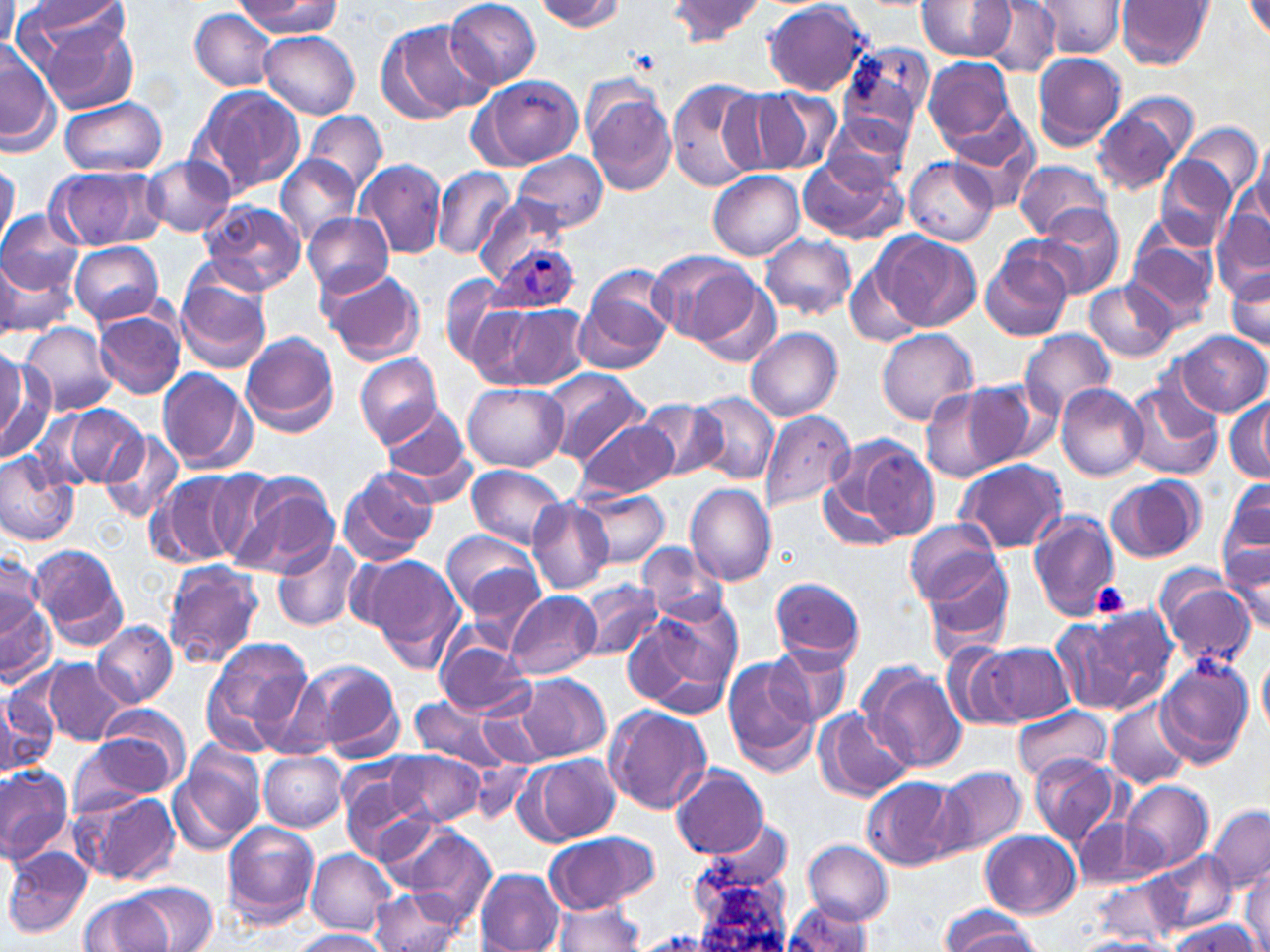

slide-level diagnosis = Plasmodium ovale
field of view = single
uninfected red blood cell locations = approximate bounding boxes as (x1,y1)-(x2,y2) corner pairs in pixels: (445,0)-(541,88), (534,0)-(626,32), (667,0)-(766,45), (1117,0)-(1213,70), (234,1)-(343,37), (917,1)-(1015,61), (980,1)-(1062,76), (1030,1)-(1125,59), (18,2)-(132,58), (763,2)-(871,95), (1243,2)-(1270,43), (189,9)-(281,92), (32,16)-(139,114), (382,18)-(492,122), (261,31)-(361,117), (0,41)-(60,158), (839,49)-(929,145), (1031,52)-(1127,151), (923,57)-(1018,149), (476,75)-(583,169), (668,79)-(766,194), (188,83)-(307,199), (582,85)-(675,198), (755,87)-(842,174), (716,88)-(802,177), (1092,95)-(1196,197), (60,97)-(169,176), (304,111)-(387,193), (821,116)-(911,190), (947,122)-(1040,211), (1182,122)-(1262,204), (1252,136)-(1270,230), (514,151)-(609,232), (798,153)-(906,245), (277,155)-(360,244), (1156,155)-(1238,252), (143,156)-(236,238), (905,157)-(998,246), (1241,157)-(1270,252), (355,158)-(448,259), (0,159)-(20,249), (1012,160)-(1113,240), (48,164)-(167,251), (432,167)-(514,260), (709,171)-(805,260), (472,196)-(570,285), (199,198)-(306,294), (1034,205)-(1126,297), (1211,208)-(1269,290), (0,210)-(85,295), (303,213)-(395,297), (874,231)-(980,332), (760,234)-(854,321), (1124,236)-(1218,332), (67,242)-(166,327), (980,248)-(1074,341), (648,249)-(757,344), (0,254)-(75,342), (844,263)-(924,350), (320,267)-(426,365), (1225,268)-(1270,353), (176,269)-(273,373), (575,270)-(674,373), (691,274)-(783,368), (441,275)-(518,365), (1085,281)-(1176,362), (474,303)-(586,392), (94,309)-(186,400), (20,322)-(118,417), (876,328)-(980,426), (746,329)-(842,422), (1020,329)-(1116,418), (1173,330)-(1267,417), (239,331)-(340,436), (0,343)-(26,448), (0,352)-(50,460), (355,353)-(442,446), (156,367)-(256,474), (544,370)-(649,466), (965,378)-(1062,467), (1123,378)-(1224,481), (462,382)-(569,470), (920,384)-(1018,480), (1056,384)-(1148,482), (692,391)-(778,483), (1224,394)-(1269,482), (636,399)-(726,481), (380,403)-(471,490), (62,405)-(149,488), (760,411)-(855,512), (576,417)-(675,499), (102,429)-(184,523), (852,442)-(940,541), (0,450)-(81,547), (956,459)-(1067,553), (464,464)-(568,549), (337,465)-(440,564), (153,470)-(250,569), (228,473)-(339,579), (1105,476)-(1205,563), (817,477)-(904,549), (1220,480)-(1270,583), (685,483)-(778,588), (577,489)-(668,568), (527,497)-(614,594), (1028,509)-(1120,619), (905,519)-(1002,604), (441,530)-(540,620), (272,538)-(362,633), (28,543)-(128,651), (638,543)-(731,626), (1220,545)-(1270,637), (921,553)-(1014,654), (365,554)-(466,672), (0,555)-(43,647), (162,561)-(264,669), (1157,574)-(1256,670), (770,576)-(864,668), (577,580)-(661,662), (0,589)-(54,682), (506,592)-(601,679), (622,605)-(739,716), (1069,611)-(1176,712), (91,619)-(177,707), (436,635)-(536,718), (203,636)-(315,746), (979,641)-(1071,726), (765,642)-(852,728), (940,642)-(1025,723), (1257,650)-(1270,734), (723,655)-(819,772), (1155,657)-(1253,766), (39,658)-(129,746), (294,659)-(406,762), (862,665)-(967,775), (519,674)-(609,760), (0,680)-(60,777), (478,694)-(551,766), (406,695)-(513,769), (1105,699)-(1192,789), (603,705)-(712,815), (1014,706)-(1110,782), (89,709)-(190,795), (818,710)-(913,798), (68,734)-(177,816), (168,748)-(266,856), (381,751)-(485,826), (258,752)-(347,832), (517,754)-(618,846), (1029,755)-(1124,848), (467,760)-(535,824), (0,763)-(74,864), (672,765)-(770,861), (934,765)-(1025,861), (339,775)-(438,862), (861,777)-(959,872), (1119,779)-(1215,874), (71,789)-(182,885), (1209,806)-(1270,891), (1072,814)-(1144,890), (222,820)-(320,926), (395,826)-(497,926), (982,831)-(1079,918), (542,832)-(659,913), (804,840)-(893,923), (3,847)-(93,940), (306,848)-(398,935), (1146,851)-(1238,935), (474,868)-(564,952), (1240,869)-(1269,952), (126,883)-(219,949), (366,884)-(471,952), (78,894)-(174,952), (783,901)-(874,952), (551,902)-(644,951), (938,903)-(1038,952), (1167,917)-(1260,951), (288,929)-(392,952), (1072,936)-(1171,951)
platelet locations = approximate bounding boxes as (x1,y1)-(x2,y2) corner pairs in pixels: (1089,582)-(1132,618)
modality = optical microscopy
magnification = 1000x
image size = 1270×952 pixels
stain = May-Grünwald-Giemsa
Plasmodium ovale-infected red blood cell locations = approximate bounding boxes as (x1,y1)-(x2,y2) corner pairs in pixels: (488,247)-(580,317)
preparation = thin blood smear